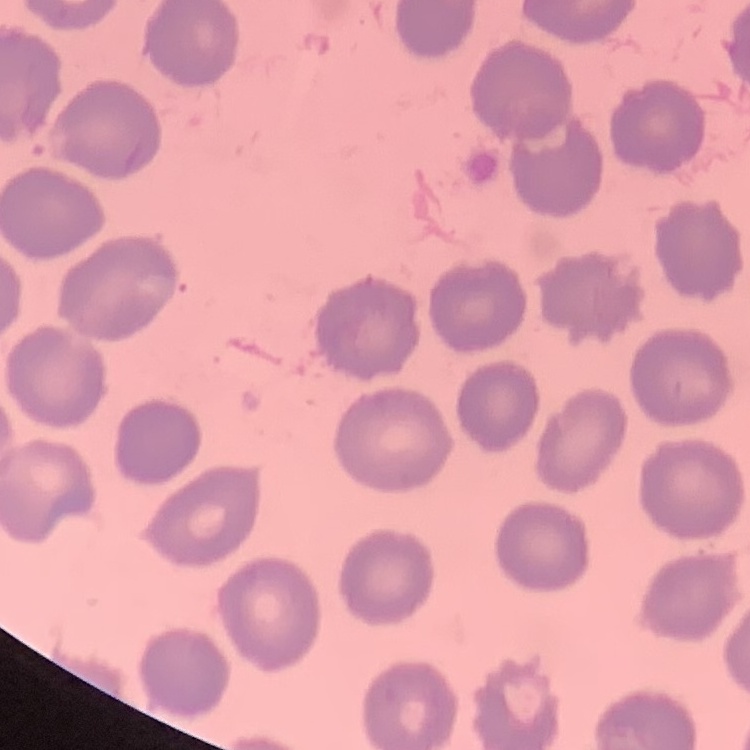
Summary:
  - Erythrocyte morphology: no rouleaux formation
  - Preparation: thin blood smear
  - Stain: Field's or Giemsa
  - Image type: square crop of a larger photomicrograph